Report the malaria status of this cell.
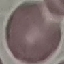

It is uninfected.

Summary:
  - Preparation: thin smear
  - Image type: cell patch, automatically extracted from a larger field of view and resized to 64 × 64 pixels
  - Capture: smartphone camera at the microscope eyepiece
  - Stain: Giemsa